Describe the morphology of the red blood cells.
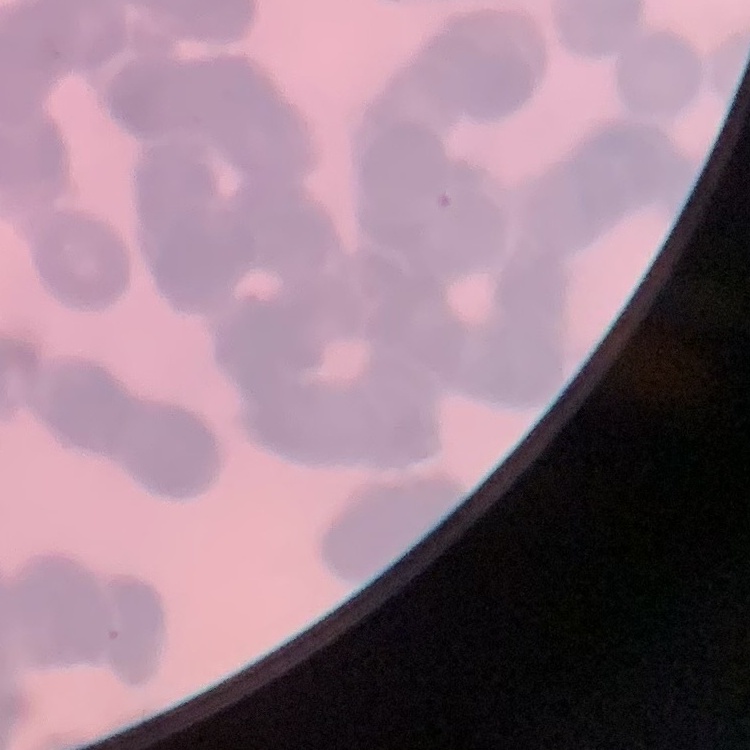

They show rouleaux formation.

preparation = thin blood film
stain = Field's or Giemsa
image type = square crop of a larger photomicrograph